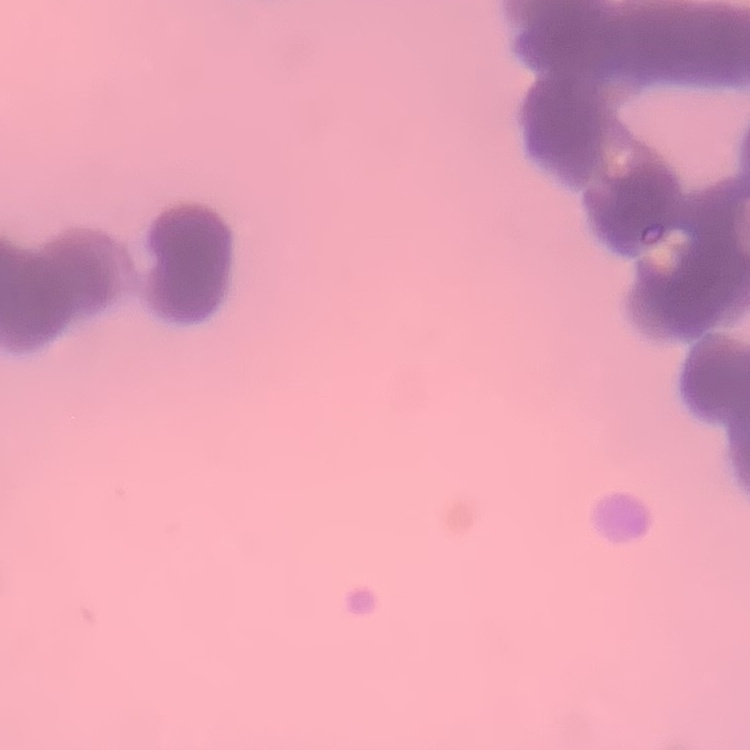
erythrocyte morphology = rouleaux formation
preparation = thin blood film
stain = Field's or Giemsa
image type = square crop of a larger photomicrograph